Comment on the morphology of the erythrocytes.
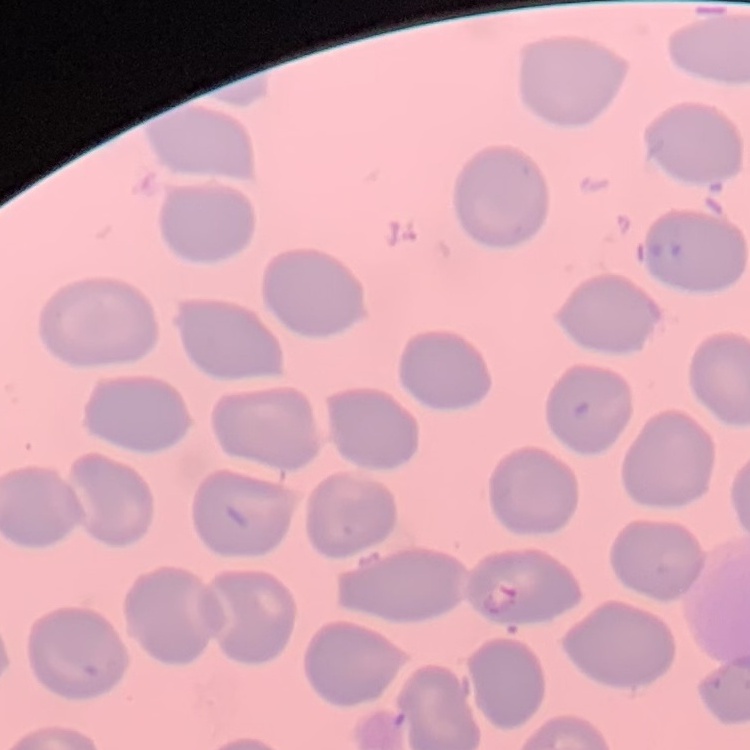
No rouleaux formation.

Summary:
  - Preparation: thin peripheral smear
  - Image type: square crop of a larger photomicrograph
  - Stain: Field's or Giemsa